Assess this cell for malaria.
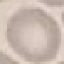

It is uninfected.

Automatically extracted cell patch, resized to 64 × 64 pixels. Giemsa-stained preparation. Photographed with a smartphone camera at the microscope eyepiece. Thin smear of blood.